Draw a bounding box around every parasitised red blood cell, every trophozoite, every gametocyte, every leukocyte, and every artifact (platelet-like body, stain precipitate, or debris).
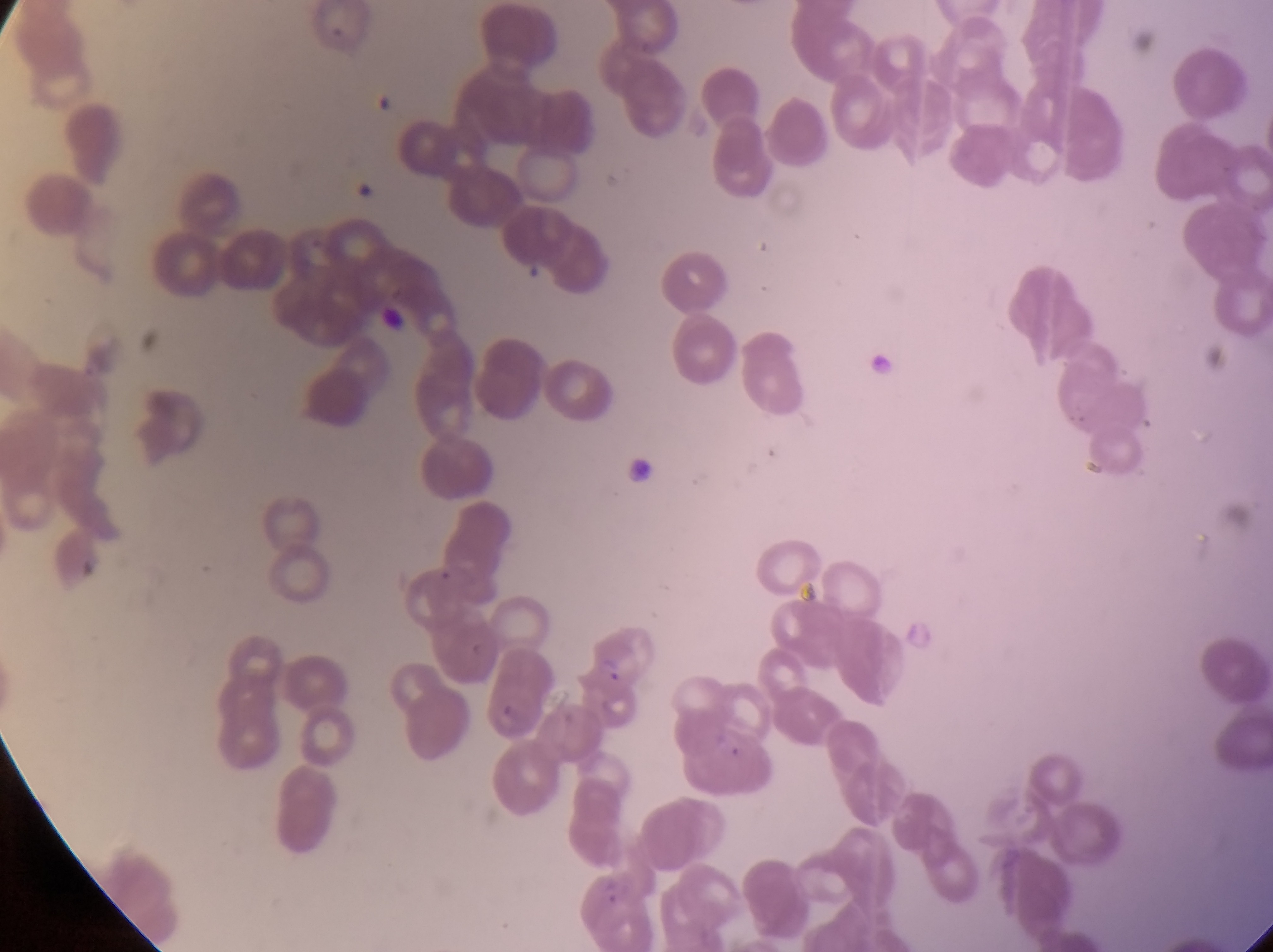
Approximate bounding boxes as left top right bottom in pixels.
Parasitised red blood cells: 571 642 649 702.
No leukocytes observed.
Artifacts (platelet-like body, stain precipitate, or debris): 350 174 373 202; 522 255 549 280; 382 294 412 341.
One object is labeled both artifact (platelet-like body, stain precipitate, or debris) and parasitised red blood cell by the source: 374 90 402 118.

capture: smartphone photograph through the eyepiece of an Olympus CX-23 microscope
magnification: 1000x
image_size: 1273×952 pixels
preparation: thin blood smear
field_of_view: single
country: Uganda